Point out each Plasmodium parasite.
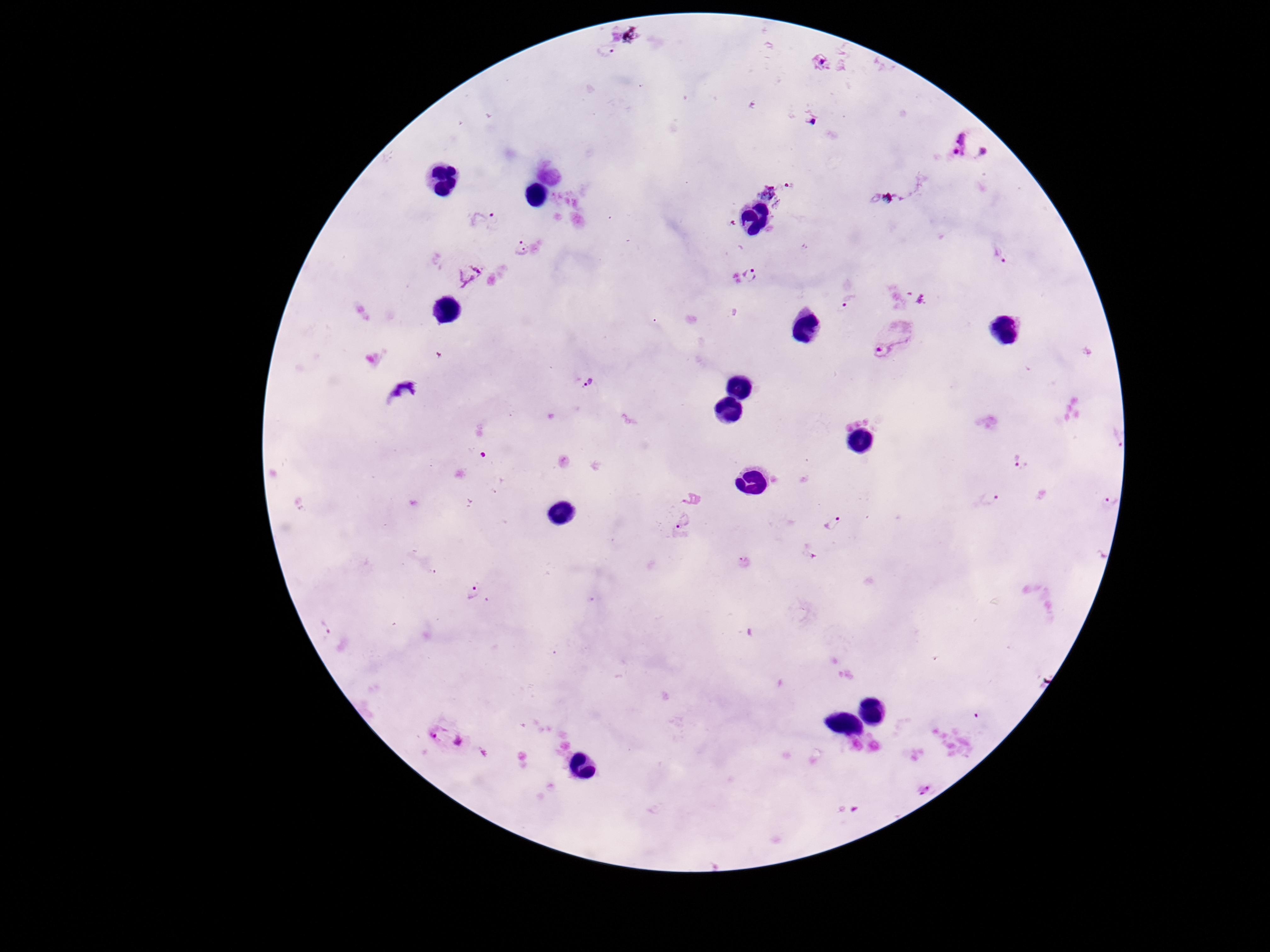
Approximate centers as {x, y} in pixels.
Plasmodium parasites: {972, 146}, {771, 197}, {484, 220}, {522, 249}, {468, 272}, {755, 275}, {845, 301}, {894, 340}, {591, 385}, {1114, 438}, {1017, 459}, {1111, 498}, {987, 500}, {682, 520}, {833, 524}, {745, 562}, {474, 591}, {323, 631}, {446, 734}, {923, 790}.

{
  "stain": "Giemsa",
  "magnification": "100x",
  "preparation": "thick blood smear",
  "capture": "smartphone camera through the microscope eyepiece",
  "patient_malaria_status": "positive",
  "field_of_view": "single",
  "image_size": "1270×952 pixels"
}